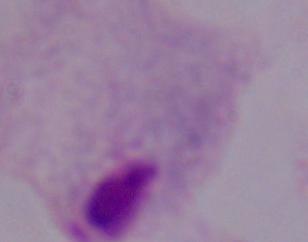

Summary:
  - Magnification: 1000x
  - Identification: trichomonad
  - Modality: photomicrograph